Assess this cell for malaria.
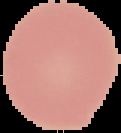
Uninfected.

Summary:
  - Image type: cell region segmented out of the field of view; surrounding area masked to black
  - Preparation: thin blood smear
  - Image size: 121×133 pixels